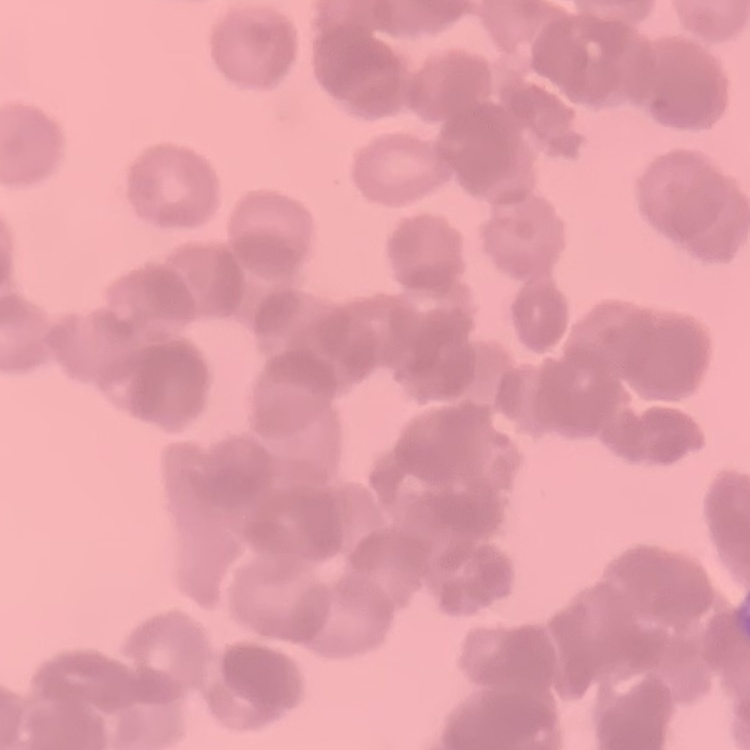 The red blood cells exhibit rouleaux formation. Thin blood film. Square crop of a larger photomicrograph. Field's or Giemsa stain.